Describe the morphology of the erythrocytes.
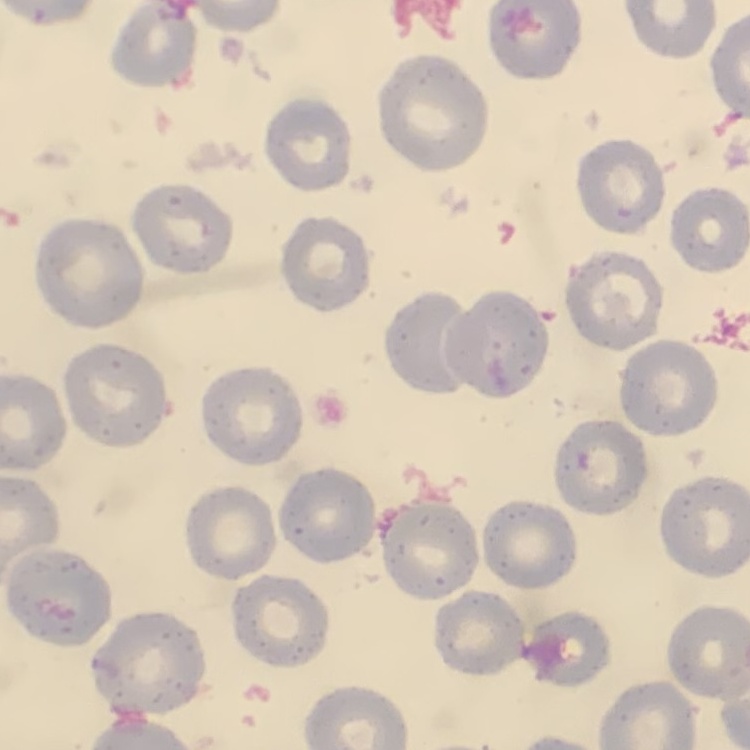

No rouleaux formation.

{
  "image_type": "square crop of a larger photomicrograph",
  "stain": "Field's or Giemsa",
  "preparation": "thin blood smear"
}